Locate the red blood cells and classify each one as P. falciparum-infected, uninfected, or of indeterminate infection status.
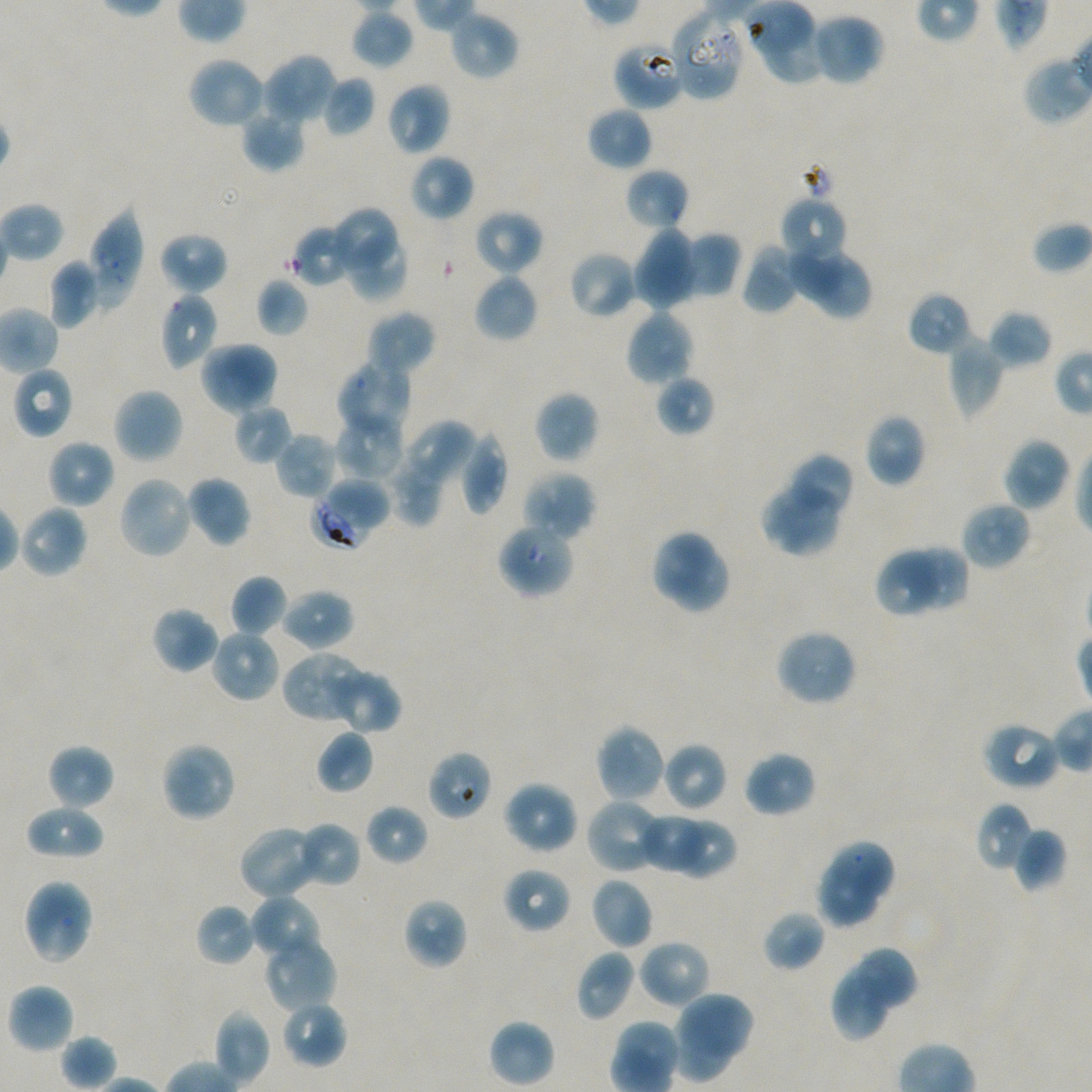

Approximate bounding boxes as {x1, y1, x2, y2} in pixels. Not every red blood cell is marked.
Infected red blood cells: {310, 495, 371, 548}.
Red blood cells of indeterminate infection status: {670, 8, 746, 101}, {613, 40, 685, 111}.
Uninfected red blood cells: {351, 10, 414, 70}, {448, 10, 520, 80}, {811, 12, 885, 86}, {759, 22, 825, 88}, {262, 52, 336, 126}, {187, 56, 266, 130}, {321, 76, 376, 137}, {386, 81, 451, 155}, {241, 105, 306, 171}, {587, 106, 653, 170}, {409, 153, 474, 221}, {625, 167, 689, 231}, {779, 196, 847, 268}, {87, 206, 143, 310}, {330, 206, 399, 275}, {473, 208, 543, 276}, {1032, 221, 1092, 274}, {291, 223, 359, 287}, {342, 227, 409, 302}, {632, 227, 700, 311}, {159, 231, 228, 294}, {683, 232, 741, 299}, {789, 235, 848, 302}, {741, 243, 802, 314}, {568, 250, 638, 319}, {806, 255, 873, 320}, {48, 259, 101, 329}, {473, 273, 539, 343}, {255, 278, 309, 337}, {907, 291, 973, 357}, {160, 293, 219, 370}, {624, 308, 695, 388}, {367, 310, 436, 377}, {989, 310, 1053, 368}, {947, 336, 1005, 418}, {199, 341, 278, 416}, {335, 361, 412, 440}, {12, 367, 73, 439}, {655, 375, 715, 436}, {112, 387, 184, 464}, {534, 391, 599, 463}, {234, 403, 293, 465}, {335, 412, 405, 481}, {864, 413, 926, 488}, {399, 419, 477, 494}, {458, 429, 508, 518}, {274, 432, 338, 500}, {1003, 437, 1071, 513}, {47, 440, 115, 509}, {386, 453, 445, 526}, {786, 453, 855, 519}, {523, 470, 596, 542}, {327, 473, 389, 528}, {118, 475, 195, 560}, {185, 475, 251, 547}, {761, 478, 843, 556}, {960, 500, 1032, 570}, {18, 504, 89, 579}, {496, 522, 576, 599}, {649, 528, 731, 615}, {909, 543, 971, 612}, {875, 544, 938, 619}, {230, 574, 289, 637}, {280, 588, 354, 650}, {151, 606, 219, 674}, {775, 628, 858, 706}, {209, 629, 280, 702}, {282, 651, 369, 725}, {327, 667, 401, 733}, {981, 721, 1061, 791}, {594, 724, 668, 803}, {315, 729, 374, 794}, {160, 741, 237, 822}, {662, 742, 727, 812}, {46, 744, 115, 810}, {426, 750, 492, 821}, {743, 751, 816, 817}, {502, 780, 579, 855}, {585, 797, 666, 875}, {975, 802, 1034, 873}, {24, 803, 105, 860}, {365, 804, 427, 864}, {640, 812, 706, 875}, {676, 816, 739, 883}, {294, 822, 361, 888}, {237, 826, 321, 899}, {1013, 827, 1068, 893}, {829, 840, 896, 903}, {815, 864, 880, 929}, {502, 867, 572, 933}, {591, 877, 654, 949}, {22, 878, 94, 965}, {249, 894, 322, 964}, {403, 897, 467, 970}, {196, 903, 258, 966}, {762, 910, 826, 972}, {263, 934, 336, 1013}, {638, 939, 712, 1009}, {858, 946, 920, 1011}, {575, 949, 636, 1023}, {829, 962, 895, 1043}, {7, 983, 75, 1055}, {679, 993, 758, 1059}, {280, 1000, 348, 1068}, {213, 1009, 270, 1086}, {670, 1018, 735, 1082}, {488, 1019, 555, 1088}, {60, 1033, 118, 1091}.

Summary:
  - Image size: 1092×1092 pixels
  - Objective: 100x, oil immersion, numerical aperture 1.45
  - Field of view: single
  - Stain: Giemsa
  - Donor blood group: A+/O+
  - Preparation: thin blood smear
  - Culture: in-vitro P. falciparum strain NF54, static